Locate every parasitized red blood cell.
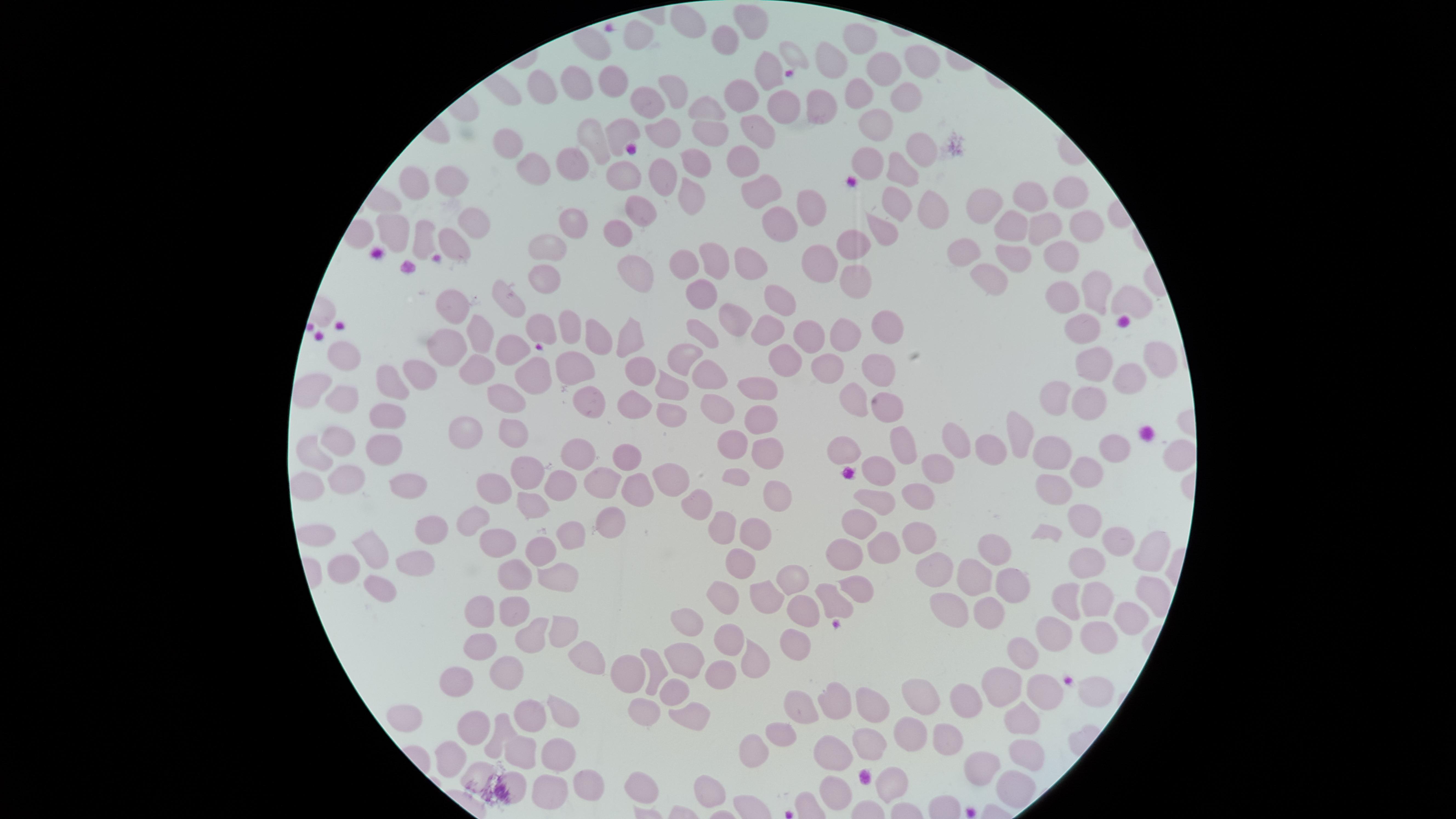

No parasitized red blood cells identified.

preparation = thin blood film
image size = 1456×819 pixels
visible region = circular
uninfected red blood cells = approximate marker points, in pixels from the top-left corner: (x=688, y=19), (x=756, y=19), (x=629, y=39), (x=730, y=39), (x=861, y=39), (x=793, y=53), (x=831, y=59), (x=919, y=63), (x=886, y=70), (x=766, y=72), (x=613, y=83), (x=575, y=84), (x=539, y=91), (x=674, y=91), (x=860, y=96), (x=906, y=100), (x=744, y=103), (x=783, y=107), (x=824, y=107), (x=647, y=108), (x=707, y=109), (x=874, y=129), (x=712, y=131), (x=621, y=133), (x=761, y=134), (x=663, y=136), (x=512, y=139), (x=599, y=145), (x=922, y=150), (x=874, y=157), (x=580, y=158), (x=743, y=159), (x=693, y=163), (x=536, y=171), (x=663, y=173), (x=901, y=173), (x=628, y=178), (x=451, y=183), (x=419, y=184), (x=759, y=189), (x=1069, y=192), (x=1027, y=196), (x=691, y=197), (x=898, y=200), (x=805, y=204), (x=987, y=204), (x=640, y=210), (x=930, y=210), (x=475, y=223), (x=577, y=223), (x=395, y=226), (x=625, y=226), (x=776, y=227), (x=882, y=228), (x=1047, y=230), (x=1012, y=232), (x=1083, y=233), (x=422, y=244), (x=854, y=245), (x=548, y=247), (x=451, y=250), (x=961, y=252), (x=1006, y=254), (x=1059, y=255), (x=814, y=258), (x=712, y=261), (x=688, y=263), (x=747, y=268), (x=635, y=270), (x=543, y=271), (x=854, y=278), (x=987, y=279), (x=1094, y=287), (x=701, y=291), (x=1066, y=299), (x=1128, y=299), (x=783, y=301), (x=454, y=306), (x=512, y=306), (x=730, y=322), (x=882, y=325), (x=569, y=327), (x=537, y=328), (x=1084, y=328), (x=765, y=330), (x=705, y=331), (x=482, y=333), (x=848, y=334), (x=596, y=338), (x=633, y=339), (x=807, y=339), (x=447, y=352), (x=505, y=352), (x=1153, y=352), (x=344, y=355), (x=1094, y=359), (x=790, y=361), (x=687, y=363), (x=878, y=367), (x=476, y=369), (x=577, y=369), (x=831, y=370), (x=640, y=372), (x=422, y=373), (x=528, y=374), (x=707, y=379), (x=1131, y=379), (x=391, y=380), (x=761, y=386), (x=672, y=388), (x=313, y=390), (x=590, y=396), (x=855, y=398), (x=511, y=400), (x=1052, y=400), (x=1087, y=400), (x=343, y=401), (x=635, y=402), (x=718, y=405), (x=885, y=407), (x=760, y=410), (x=387, y=412), (x=669, y=412), (x=475, y=431), (x=513, y=431), (x=1013, y=432), (x=337, y=438), (x=906, y=440), (x=737, y=442), (x=962, y=442), (x=381, y=444), (x=852, y=446), (x=773, y=447), (x=629, y=449), (x=993, y=449), (x=310, y=451), (x=1049, y=453), (x=577, y=455), (x=940, y=468), (x=532, y=471), (x=669, y=472), (x=882, y=472), (x=1087, y=472), (x=344, y=475), (x=607, y=476), (x=735, y=476), (x=1057, y=480), (x=558, y=481), (x=308, y=486), (x=409, y=489), (x=496, y=489), (x=637, y=491), (x=773, y=494), (x=775, y=496), (x=871, y=500), (x=912, y=500), (x=527, y=505), (x=701, y=505), (x=470, y=519), (x=855, y=519), (x=1075, y=519), (x=607, y=523), (x=431, y=532), (x=561, y=532), (x=321, y=533), (x=758, y=533), (x=723, y=535), (x=907, y=540), (x=491, y=542), (x=1115, y=545), (x=991, y=547), (x=874, y=551), (x=374, y=552), (x=840, y=557), (x=1158, y=557), (x=740, y=558), (x=540, y=563), (x=940, y=563), (x=1088, y=563), (x=349, y=567), (x=411, y=568), (x=976, y=576), (x=560, y=580), (x=800, y=581), (x=1008, y=583), (x=512, y=584), (x=851, y=587), (x=1141, y=590), (x=380, y=593), (x=769, y=594), (x=1061, y=596), (x=724, y=600), (x=1089, y=602), (x=831, y=603), (x=510, y=605), (x=478, y=608), (x=952, y=610), (x=797, y=615), (x=987, y=615), (x=1122, y=623), (x=565, y=628), (x=688, y=630), (x=1045, y=635), (x=722, y=637), (x=1094, y=637), (x=534, y=638), (x=791, y=648), (x=482, y=649), (x=1021, y=653), (x=751, y=659), (x=593, y=662), (x=683, y=662), (x=655, y=671), (x=631, y=676), (x=722, y=676), (x=509, y=680), (x=1005, y=680), (x=459, y=681), (x=1044, y=690), (x=1085, y=691), (x=673, y=699), (x=868, y=701), (x=917, y=701), (x=959, y=702), (x=800, y=705), (x=836, y=705), (x=643, y=711), (x=406, y=714), (x=530, y=719), (x=688, y=719), (x=1016, y=719), (x=565, y=725), (x=498, y=732), (x=779, y=732), (x=473, y=733), (x=908, y=739), (x=745, y=744), (x=861, y=744), (x=940, y=746), (x=1019, y=748), (x=828, y=755), (x=519, y=758), (x=558, y=758), (x=452, y=760), (x=990, y=760), (x=484, y=776), (x=895, y=781), (x=1011, y=781), (x=513, y=782), (x=583, y=783), (x=644, y=790), (x=829, y=790), (x=544, y=796), (x=706, y=797)
capture = smartphone photograph through the microscope eyepiece
stain = Giemsa
field of view = single